Assess this cell for malaria.
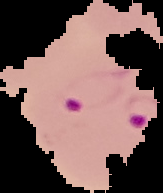
It is parasitized.

preparation: thin blood smear
image_type: segmented cell region with the area outside set to black
image_size: 163×193 pixels